Assess this cell for malaria.
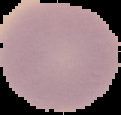
It is uninfected.

image size = 121×115 pixels
image type = cell region segmented out of the field of view; surrounding area masked to black
preparation = thin blood film